State the preparation type.
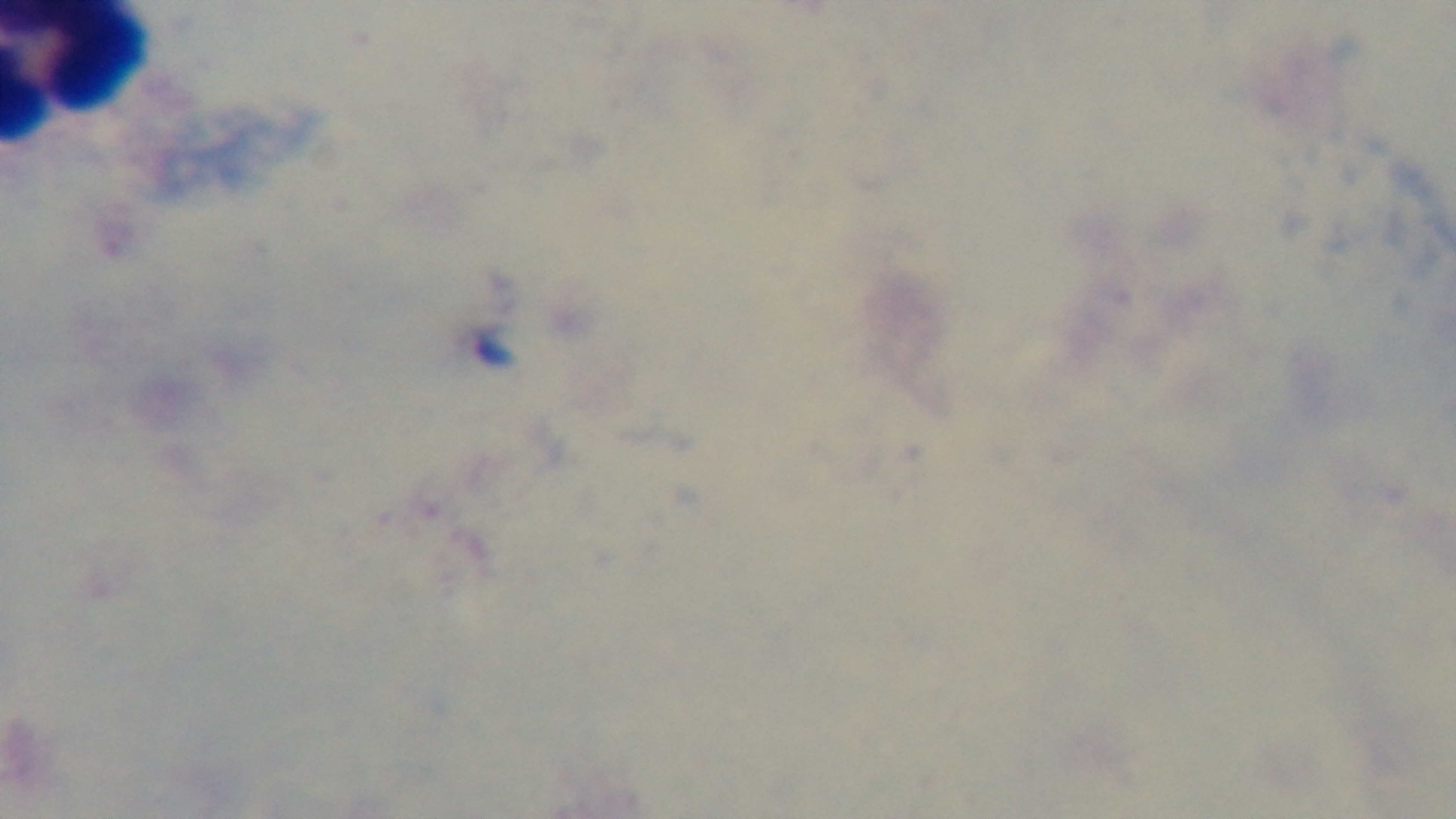
It is a thick blood film.

Summary:
  - Modality: light microscopy
  - Objective: 100x oil immersion
  - Stain: Giemsa
  - Malaria status: negative
  - Field of view: single
  - Capture: mounted 4K digital camera